Assess this cell for malaria.
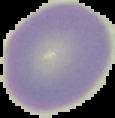

It is uninfected.

From a thin blood smear. Segmented cell region on a black background. Image is 115×118 pixels.